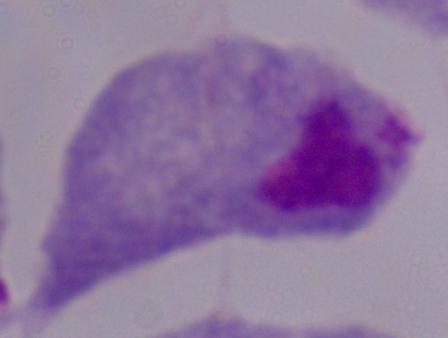

Summary:
  - Magnification: 1000x
  - Identification: trichomonad
  - Modality: micrograph